Assess the morphology of the red blood cells.
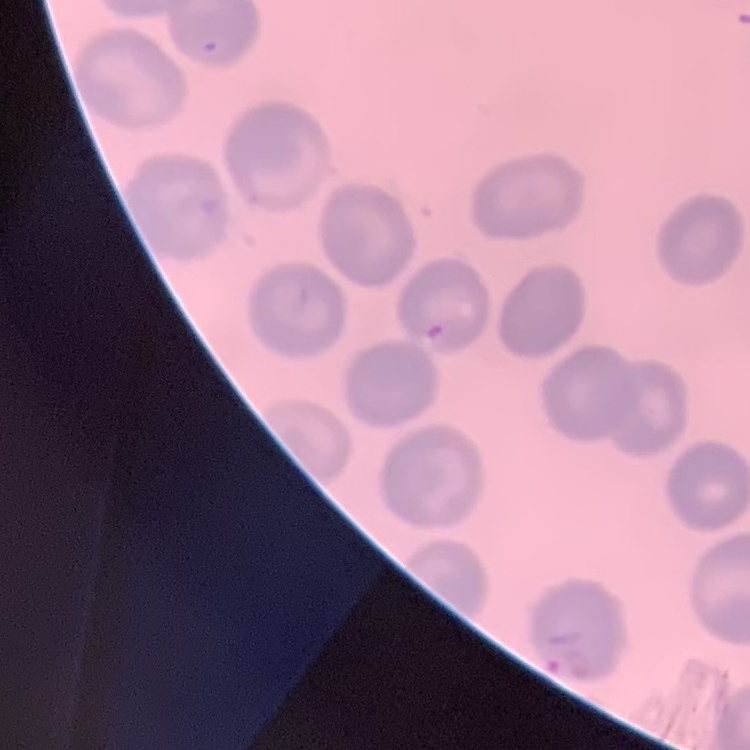
No rouleaux formation.

Thin peripheral smear. Field's or Giemsa stain. Square crop of a larger photomicrograph.